Classify this cell by malaria status.
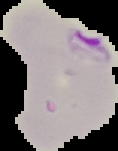

It is parasitized.

image type = cell region segmented out of the field of view; surrounding area masked to black
preparation = thin blood smear
image size = 118×151 pixels